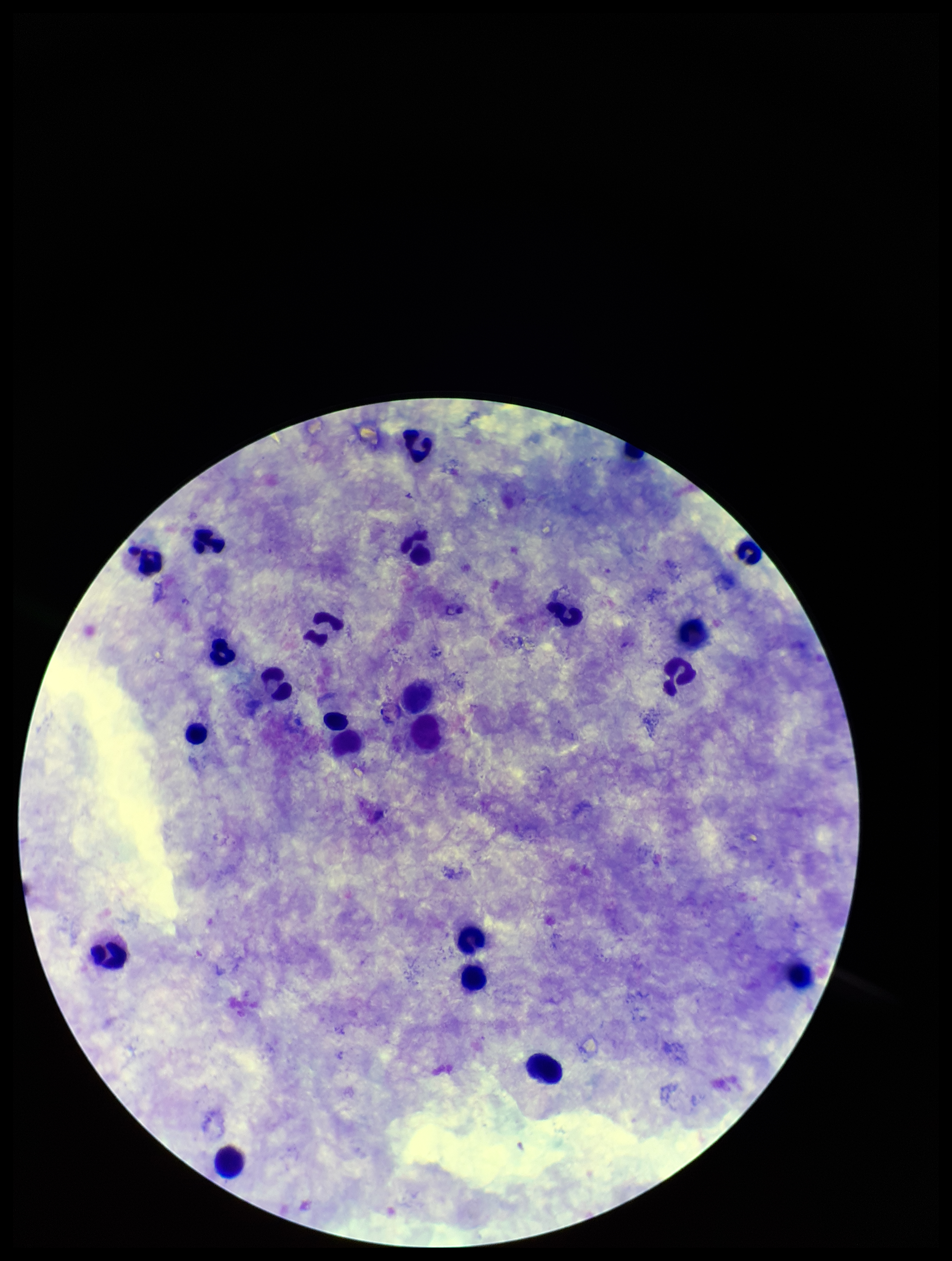

Summary:
  - Plasmodium parasites: none detected
  - Capture: smartphone photograph through the microscope eyepiece
  - Parasite count: 0
  - Preparation: thick blood smear
  - Stain: Giemsa
  - Leukocyte count: 19
  - Image size: 952×1261 pixels
  - Field of view: single
  - Patient malaria status: negative